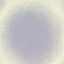

{
  "malaria_status": "uninfected",
  "preparation": "thin blood smear",
  "capture": "smartphone through the microscope eyepiece",
  "image_type": "automatically extracted cell patch, resized to 64 × 64 pixels",
  "stain": "Giemsa"
}